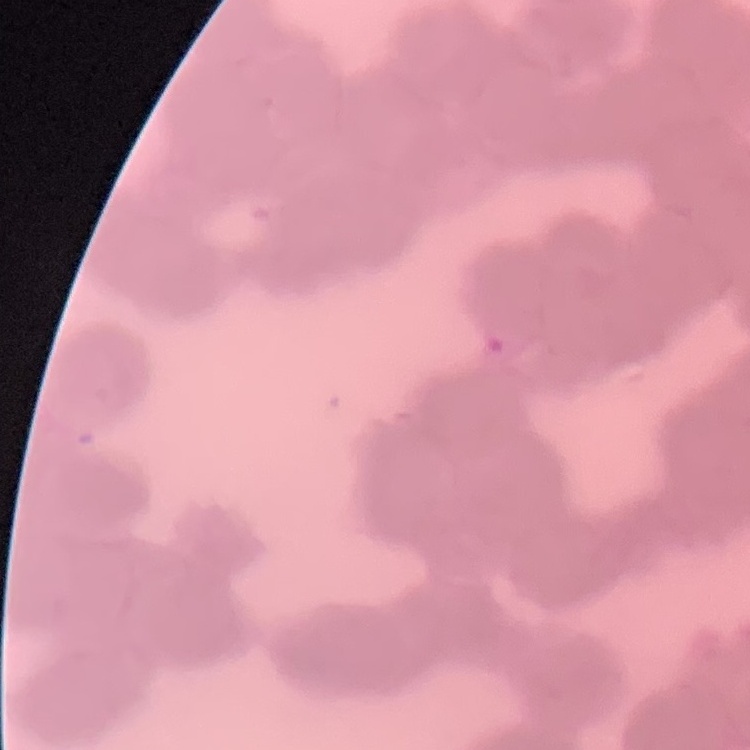

erythrocyte morphology = rouleaux formation
preparation = thin blood smear
stain = Field's or Giemsa
image type = square crop of a larger photomicrograph